Assess this cell for malaria.
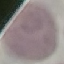
It is uninfected.

Giemsa stain. Thin blood film. Cell patch, automatically extracted from a larger field of view and resized to 64 × 64 pixels. Acquired by smartphone through the microscope eyepiece.